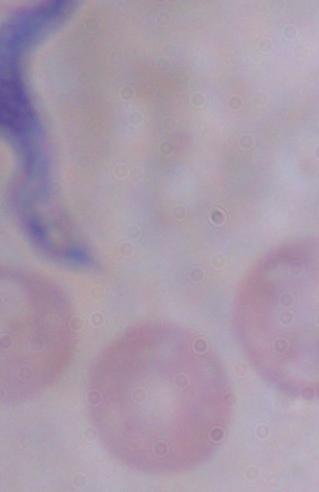
1000x magnification. A trypanosome is seen. Photomicrograph.